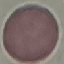

Summary:
  - Result: no malaria parasites seen
  - Preparation: thin blood smear
  - Capture: smartphone camera at the microscope eyepiece
  - Image type: automatically extracted cell patch, resized to 64 × 64 pixels
  - Stain: Giemsa